Outline each uninfected red blood cell.
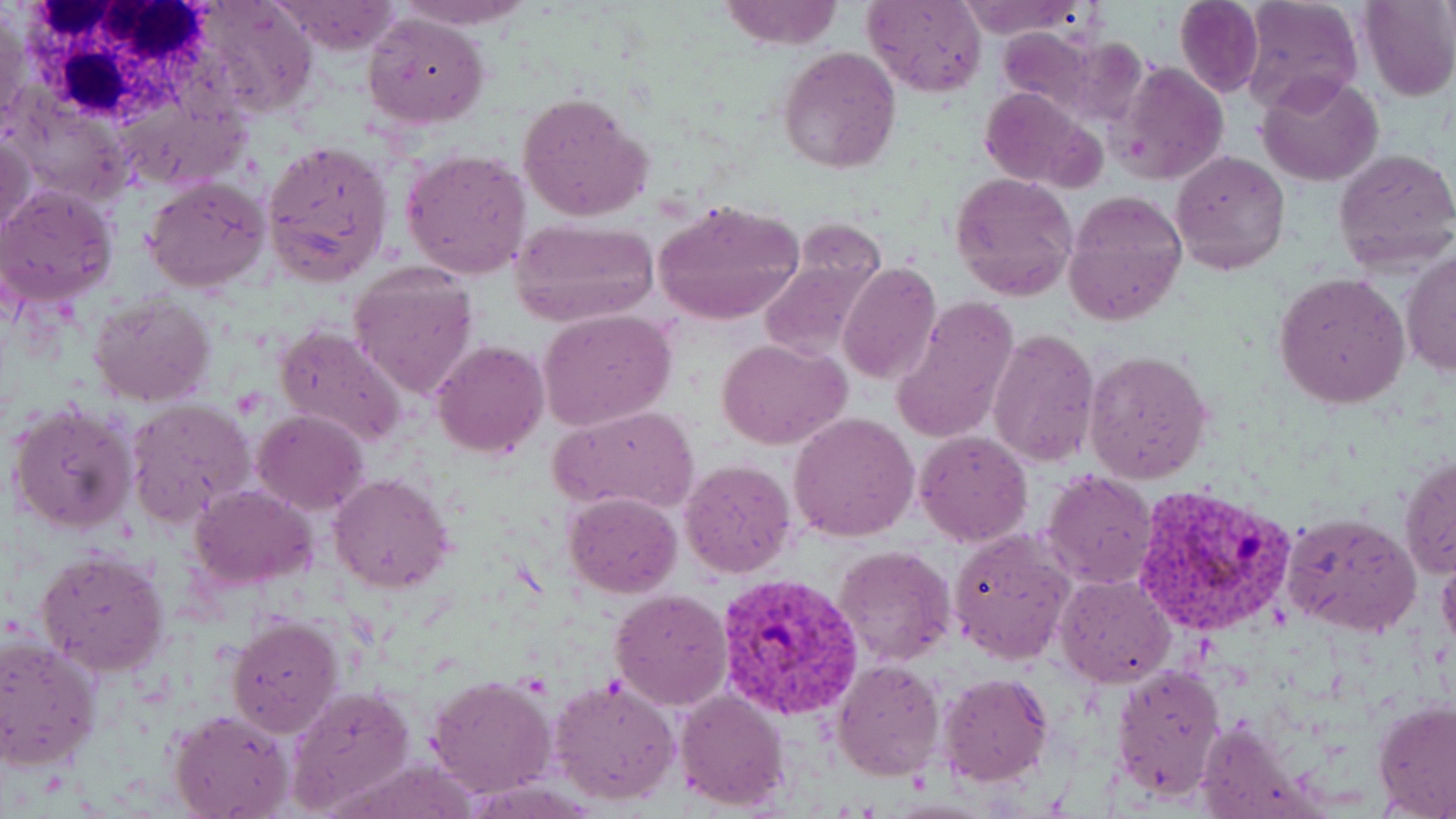

Approximate bounding boxes as (x1,y1)-(x2,y2) corner pairs in pixels.
Uninfected red blood cells: (187,0)-(319,121), (272,0)-(404,55), (393,0)-(533,30), (718,0)-(843,48), (865,0)-(984,97), (955,0)-(1085,39), (1174,0)-(1265,98), (1239,0)-(1361,112), (1359,0)-(1456,101), (0,10)-(27,128), (361,13)-(489,129), (994,25)-(1104,117), (779,45)-(902,175), (1116,60)-(1230,187), (1257,72)-(1383,187), (1141,81)-(1259,228), (979,90)-(1100,189), (517,93)-(653,222), (1,131)-(35,238), (264,138)-(395,283), (1332,146)-(1456,271), (401,150)-(532,279), (1171,150)-(1290,275), (948,173)-(1077,299), (142,177)-(270,293), (0,185)-(119,306), (1063,187)-(1186,326), (651,199)-(804,325), (509,216)-(661,326), (1402,252)-(1455,375), (756,256)-(883,363), (837,262)-(941,386), (348,267)-(480,401), (1273,272)-(1410,410), (89,293)-(217,406), (892,294)-(1019,445), (539,310)-(676,431), (273,322)-(406,449), (987,327)-(1099,466), (718,338)-(851,450), (431,339)-(547,459), (1084,349)-(1213,483), (125,399)-(256,530), (7,401)-(137,535), (553,405)-(698,514), (253,410)-(369,515), (789,410)-(920,542), (914,431)-(1032,547), (1399,453)-(1456,578), (679,458)-(797,580), (1043,469)-(1157,587), (330,473)-(455,592), (189,484)-(318,590), (565,492)-(682,597), (1283,512)-(1421,636), (948,528)-(1075,665), (836,544)-(958,667), (35,551)-(170,677), (1438,554)-(1456,656), (1056,574)-(1177,690), (610,588)-(732,710), (226,614)-(342,736), (0,635)-(100,770), (832,659)-(946,781), (1111,663)-(1227,799), (939,672)-(1053,785), (427,675)-(556,798), (548,679)-(681,806), (287,685)-(416,813), (675,689)-(789,811), (1371,699)-(1456,819), (169,710)-(292,819), (1196,716)-(1316,819).

White blood cell locations: (23,0)-(210,134). Plasmodium vivax-infected red blood cell locations: (1133,482)-(1297,637), (717,571)-(864,724). Slide-level diagnosis: Plasmodium vivax. Thin blood film. One field of a larger specimen. Image is 1456×819 pixels. Light microscopy. Captured at 1000x magnification. May-Grünwald-Giemsa stain.